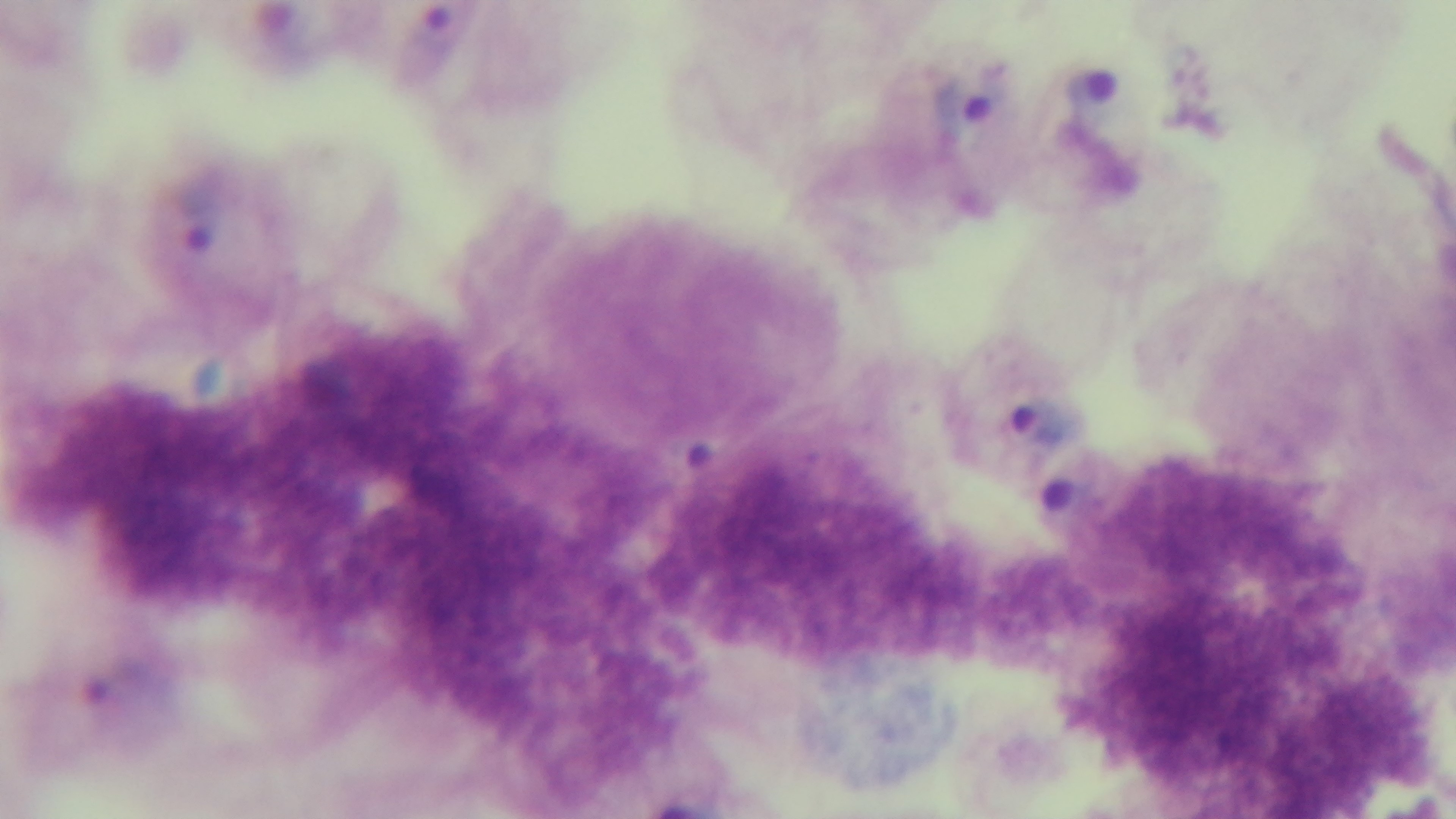

Summary:
  - Field of view: single
  - Objective: 100x oil immersion
  - Capture: mounted 4K digital camera
  - Preparation: thick
  - Malaria status: positive
  - Stain: Giemsa
  - Modality: light microscopy